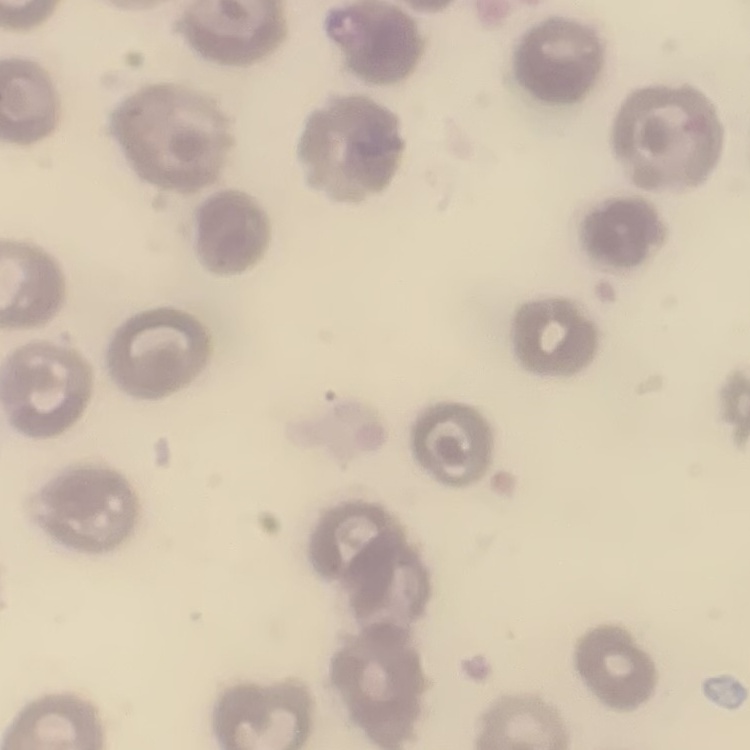
erythrocyte morphology = no rouleaux formation
preparation = thin peripheral smear
image type = square crop of a larger photomicrograph
stain = Field's or Giemsa